Report the malaria status of this cell.
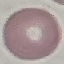

Uninfected.

Summary:
  - Preparation: thin blood film
  - Image type: cell patch, automatically extracted from a larger field of view and resized to 64 × 64 pixels
  - Capture: smartphone through the microscope eyepiece
  - Stain: Giemsa